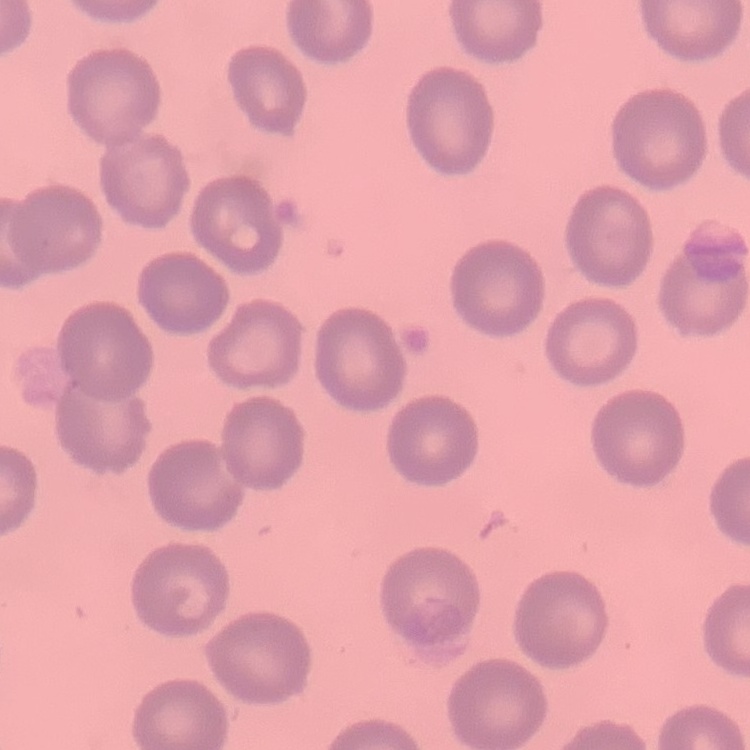

{
  "red_blood_cell_morphology": "no rouleaux formation",
  "preparation": "thin blood smear",
  "stain": "Field's or Giemsa",
  "image_type": "one tile cut from a larger photomicrograph"
}